Name the parasite shown.
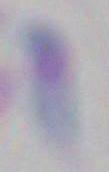

Toxoplasma gondii.

Photomicrograph. Captured at 1000x magnification.